Describe the morphology of the red blood cells.
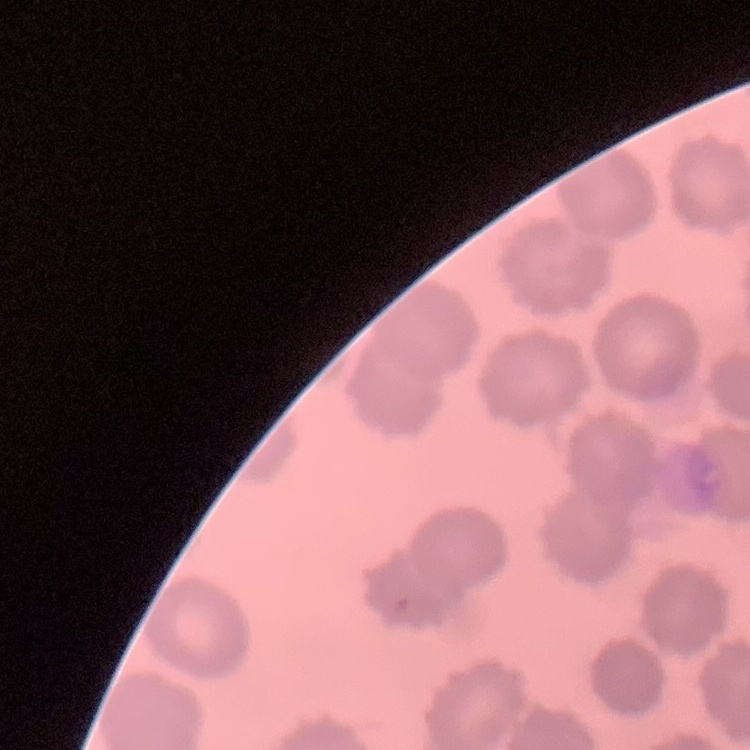
They show no rouleaux formation.

preparation = thin blood film
image type = one tile cut from a larger photomicrograph
stain = Field's or Giemsa